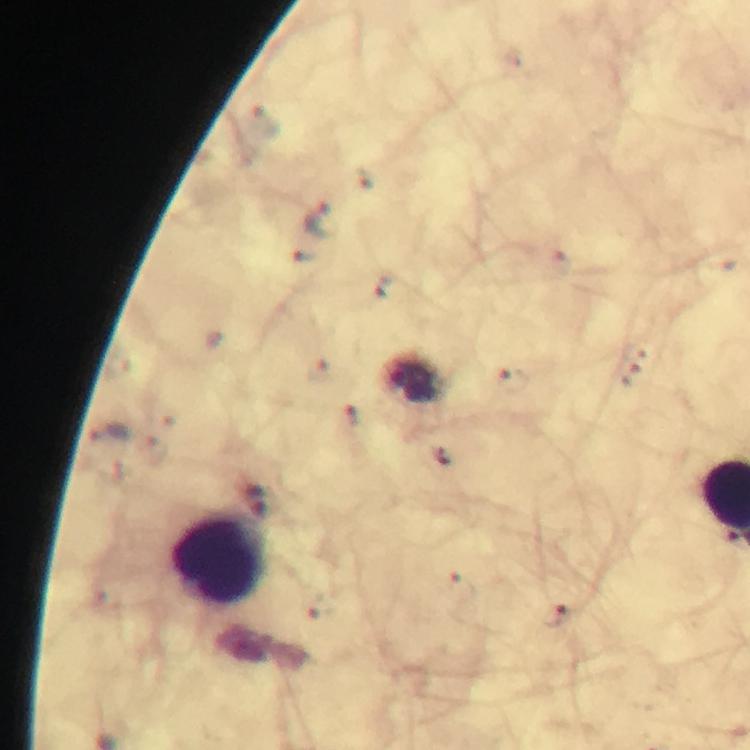

{
  "leukocyte_locations": "approximate centers as (x, y) in pixels: (218, 558)",
  "image_size": "750×750 pixels",
  "immersion_oil": "used",
  "stain": "Giemsa",
  "preparation": "thick blood smear",
  "malaria_parasite_locations": "approximate centers as (x, y) in pixels: (321, 220), (383, 287), (353, 417), (110, 436), (444, 459), (466, 585), (323, 608), (555, 621)",
  "magnification": "100x",
  "cropped_from": "a single field of view",
  "capture": "smartphone mounted on the microscope",
  "context": "from a malaria diagnostic workup"
}